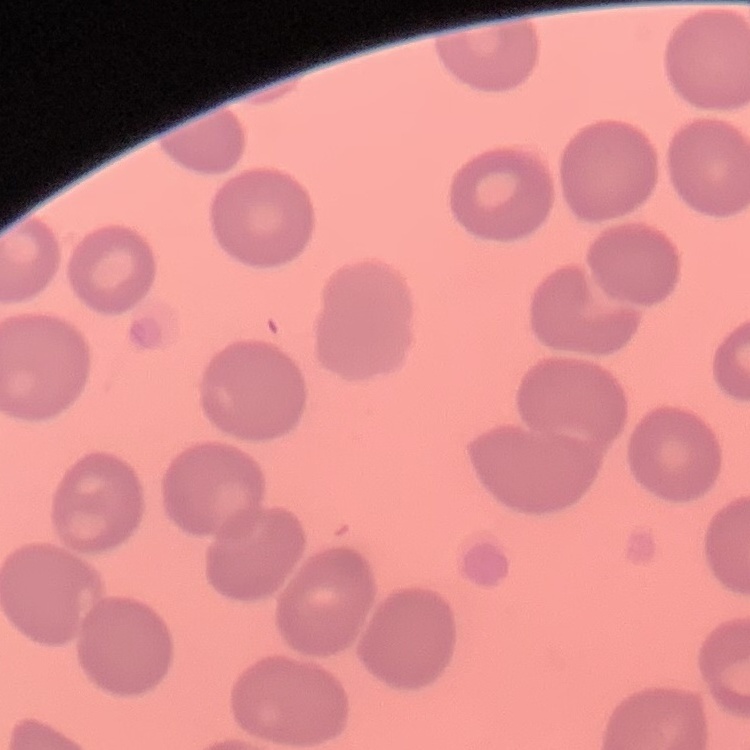
red blood cell morphology = no rouleaux formation
preparation = thin blood film
stain = Field's or Giemsa
image type = one tile cut from a larger photomicrograph